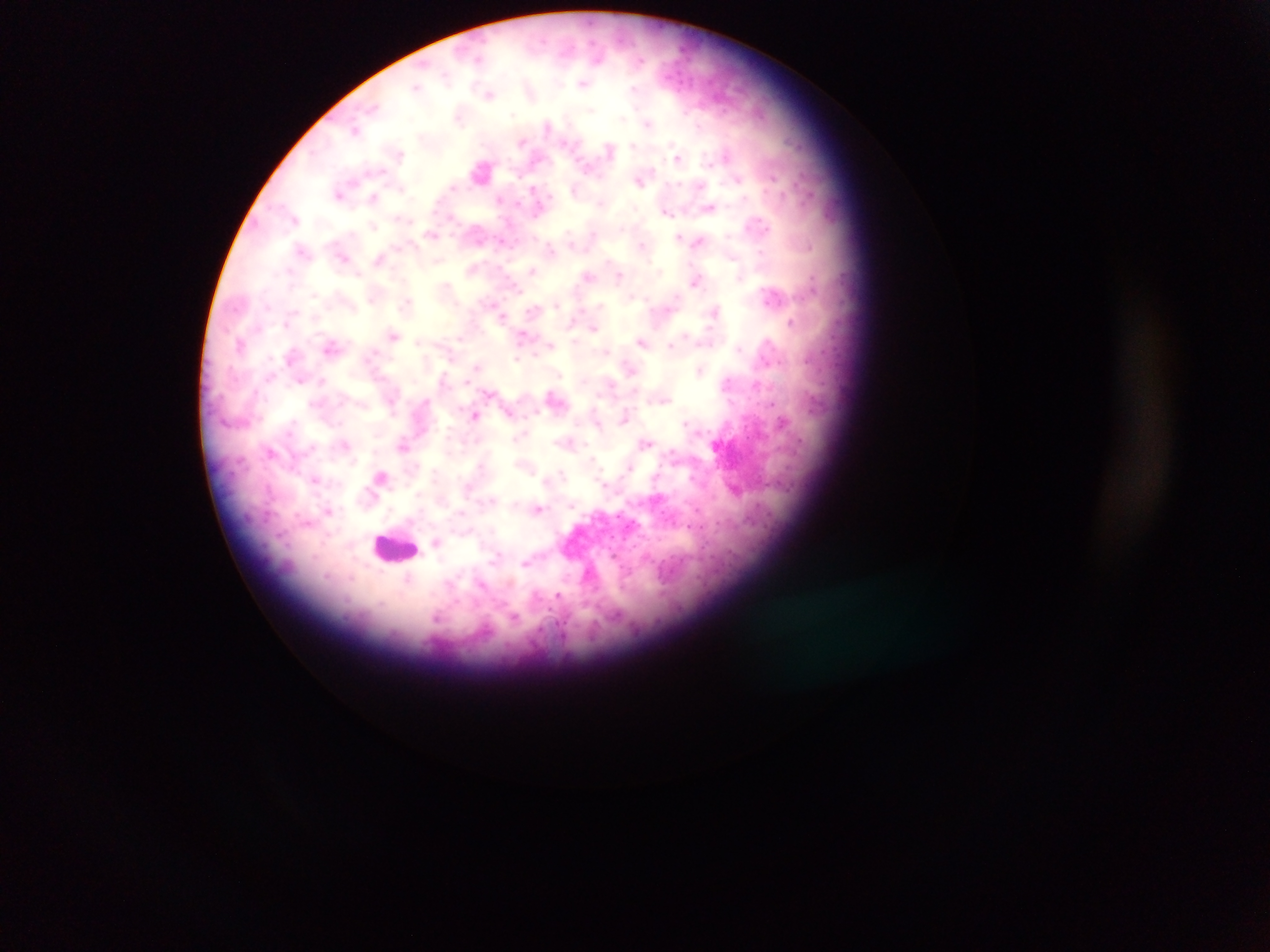
Approximate centers as {x, y} in pixels. Leukocyte locations: {396, 548}. Malaria parasite locations: {599, 57}, {478, 58}, {640, 60}, {446, 76}, {582, 84}, {416, 87}, {634, 89}, {531, 90}, {490, 93}, {372, 107}, {590, 110}, {458, 117}, {622, 118}, {648, 124}, {548, 125}, {356, 130}, {522, 142}, {634, 145}, {610, 149}, {399, 154}, {727, 154}, {678, 157}, {482, 171}, {382, 172}, {773, 177}, {738, 179}, {639, 180}, {700, 186}, {453, 187}, {533, 189}, {339, 195}, {374, 197}, {500, 198}, {601, 203}, {710, 207}, {667, 213}, {294, 218}, {373, 225}, {763, 226}, {622, 228}, {431, 234}, {592, 234}, {679, 236}, {728, 236}, {698, 241}, {642, 244}, {809, 246}, {550, 249}, {301, 250}, {761, 252}, {344, 257}, {379, 258}, {438, 260}, {659, 270}, {532, 271}, {358, 274}, {588, 275}, {619, 276}, {696, 281}, {446, 286}, {515, 286}, {314, 295}, {772, 296}, {371, 300}, {406, 302}, {268, 305}, {556, 305}, {599, 305}, {714, 312}, {502, 316}, {791, 322}, {285, 323}, {594, 328}, {523, 334}, {393, 335}, {460, 337}, {642, 341}, {768, 341}, {419, 342}, {240, 343}, {331, 345}, {551, 345}, {671, 345}, {738, 348}, {518, 359}, {476, 368}, {630, 368}, {699, 371}, {299, 381}, {322, 381}, {467, 381}, {727, 382}, {611, 384}, {754, 386}, {490, 393}, {660, 400}, {772, 403}, {536, 412}, {510, 413}, {475, 416}, {625, 416}, {784, 422}, {684, 423}, {522, 435}, {517, 438}, {567, 443}, {647, 443}, {345, 446}, {403, 446}, {270, 451}, {673, 453}, {592, 459}, {629, 466}, {562, 474}, {316, 479}, {546, 479}, {604, 485}, {268, 488}, {418, 495}, {492, 499}, {571, 505}, {538, 509}, {329, 511}, {461, 512}, {306, 522}, {436, 542}, {498, 555}, {525, 563}, {480, 584}, {557, 596}, {438, 617}, {513, 617}. One field of view. Image is 1270×952 pixels. Thick blood smear. Sample from Ghana. Mobile-phone photograph taken through the microscope.